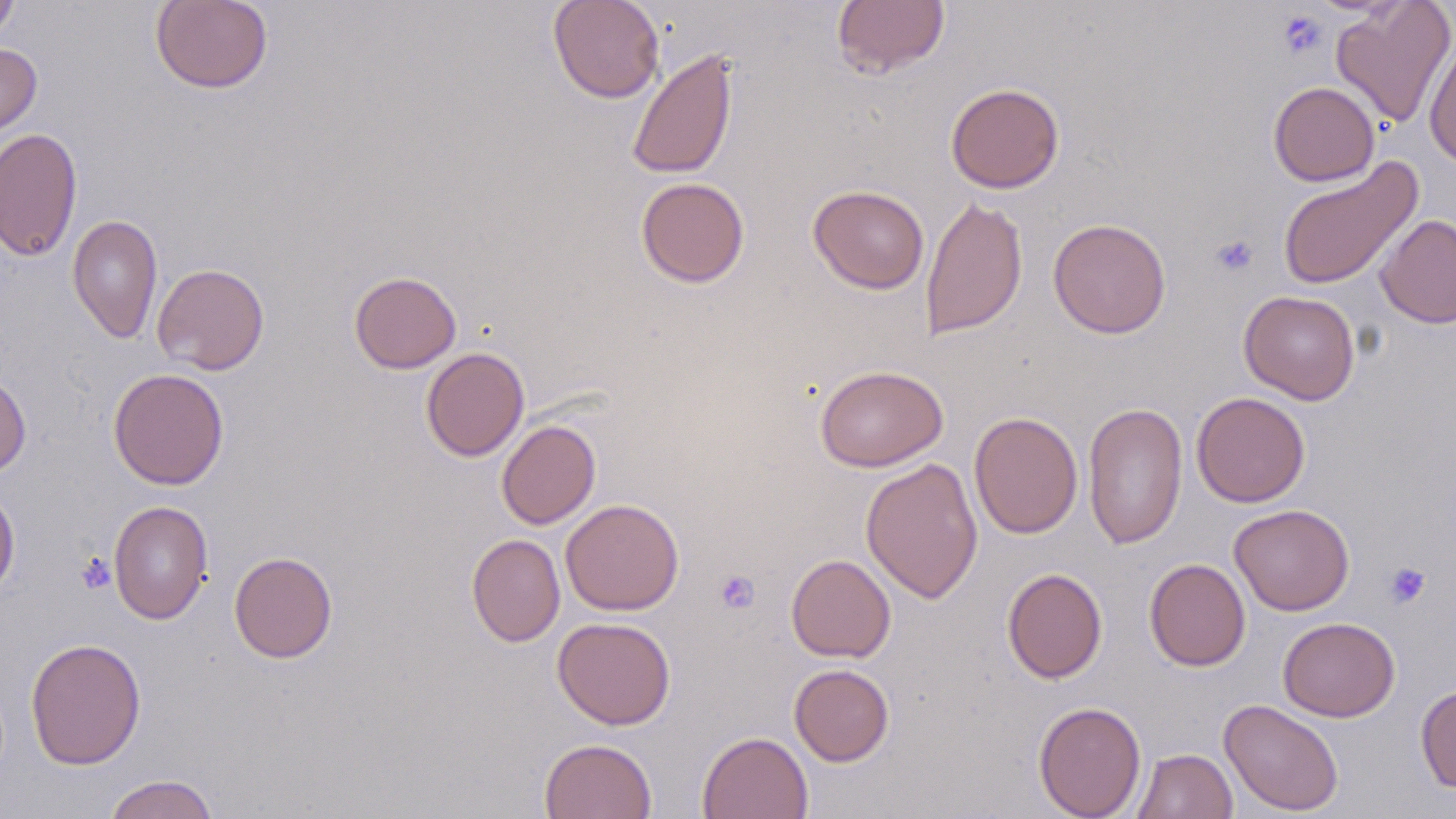

Summary:
  - Coordinate format: approximate bounding boxes as (x1, y1, x2, y2) in pixels
  - Platelet locations: (1277, 10, 1327, 60), (1210, 234, 1259, 278), (76, 553, 116, 594), (1383, 561, 1431, 609), (714, 569, 760, 615)
  - Uninfected red blood cell locations: (548, 0, 665, 103), (831, 0, 950, 79), (0, 1, 19, 44), (150, 1, 273, 94), (1331, 1, 1456, 128), (1424, 38, 1456, 169), (0, 43, 41, 138), (626, 47, 738, 180), (1268, 81, 1379, 186), (945, 83, 1065, 193), (0, 127, 82, 262), (1277, 157, 1423, 292), (636, 177, 750, 288), (808, 184, 930, 294), (920, 194, 1028, 340), (1375, 213, 1456, 328), (67, 214, 163, 344), (1048, 218, 1172, 339), (152, 263, 269, 375), (349, 270, 462, 374), (1239, 290, 1360, 405), (420, 347, 529, 462), (814, 364, 948, 472), (108, 368, 230, 490), (0, 370, 31, 479), (1191, 392, 1310, 507), (1083, 402, 1187, 549), (969, 411, 1084, 539), (497, 420, 601, 529), (860, 458, 984, 604), (0, 482, 20, 601), (560, 498, 684, 615), (108, 500, 212, 625), (1229, 504, 1354, 616), (466, 534, 565, 646), (229, 551, 338, 663), (786, 553, 896, 662), (1144, 558, 1250, 671), (1002, 568, 1107, 683), (552, 616, 677, 730), (1277, 617, 1400, 722), (25, 637, 146, 769), (789, 663, 895, 766), (1415, 684, 1456, 794), (1219, 698, 1344, 816), (1033, 700, 1146, 819), (697, 731, 813, 819), (539, 738, 657, 819), (1131, 748, 1238, 819), (104, 774, 219, 819)
  - Slide-level diagnosis: negative for blood parasites
  - Field of view: single
  - Image size: 1456×819 pixels
  - Stain: May-Grünwald-Giemsa
  - Magnification: 1000x
  - Modality: optical microscopy
  - Preparation: thin blood smear